Name the parasite shown.
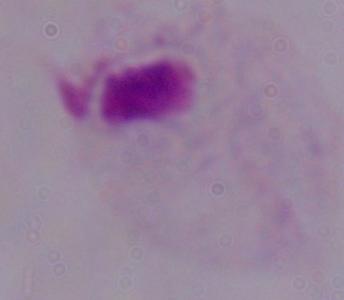
This is a trichomonad.

Summary:
  - Magnification: 1000x
  - Modality: micrograph